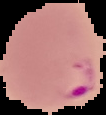
{
  "preparation": "thin blood smear",
  "image_type": "segmented cell region with the area outside set to black",
  "malaria_status": "parasitized",
  "image_size": "106×115 pixels"
}